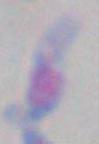
magnification = 1000x
identification = Toxoplasma gondii
modality = photomicrograph